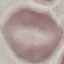
Result: no malaria parasites detected. Cell patch, automatically extracted from a larger field of view and resized to 64 × 64 pixels. Photographed with a smartphone camera at the microscope eyepiece. Giemsa-stained preparation. Thin blood smear.